Classify this cell by malaria status.
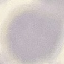

Uninfected.

Summary:
  - Image type: automatically extracted cell patch, resized to 64 × 64 pixels
  - Stain: Giemsa
  - Capture: smartphone camera at the microscope eyepiece
  - Preparation: thin smear